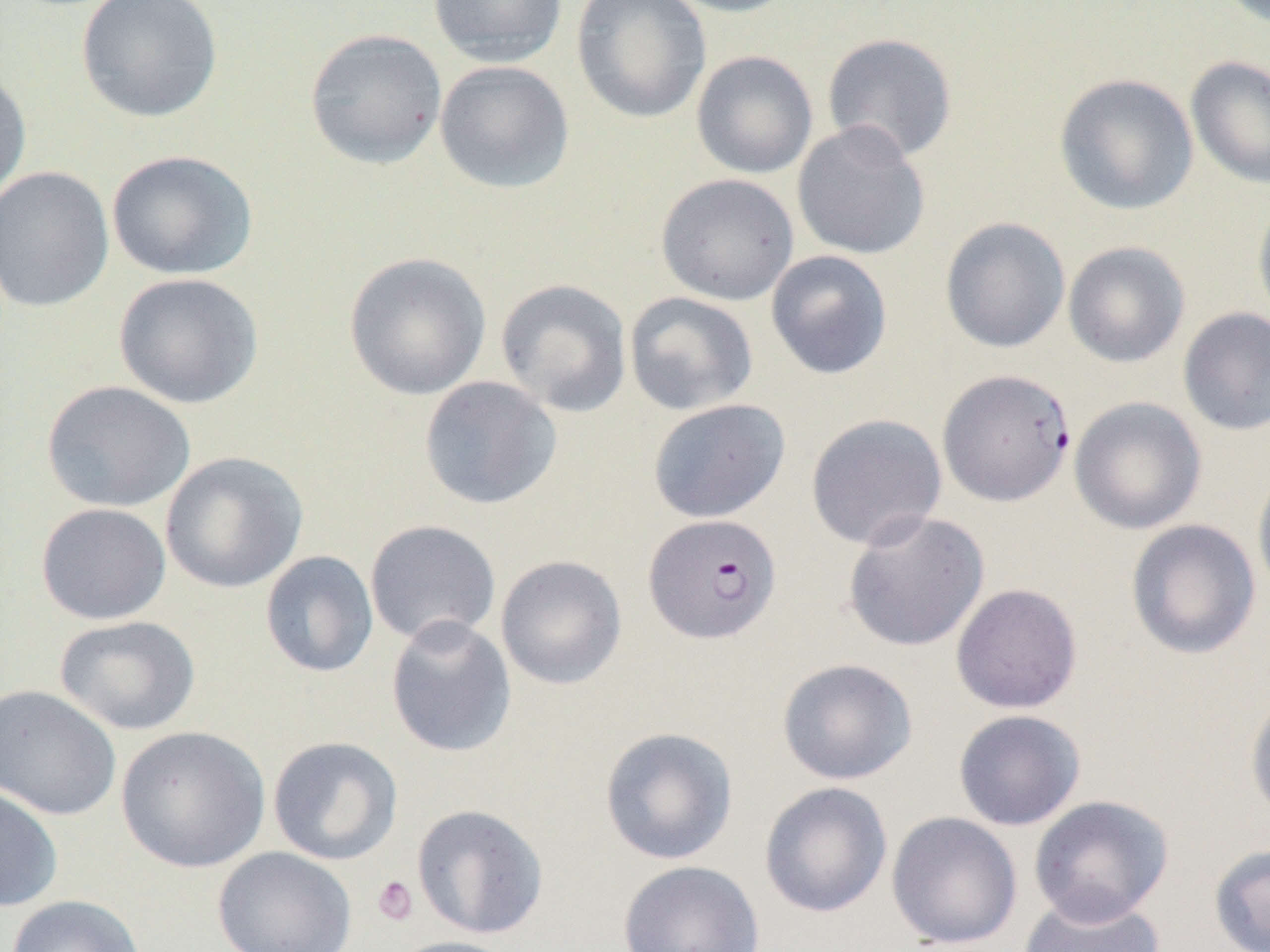
{
  "slide_level_diagnosis": "Plasmodium falciparum",
  "uninfected_red_blood_cell_locations": "approximate bounding boxes as [x1, y1, x2, y2] in pixels: [75, 0, 223, 123], [428, 0, 567, 67], [571, 0, 711, 125], [657, 0, 800, 18], [304, 28, 448, 169], [821, 32, 958, 163], [691, 50, 818, 179], [1185, 55, 1270, 190], [434, 60, 575, 195], [0, 64, 32, 205], [1054, 73, 1199, 216], [792, 121, 931, 260], [106, 149, 258, 281], [0, 166, 115, 313], [655, 173, 799, 306], [1252, 193, 1270, 330], [939, 217, 1071, 353], [1063, 241, 1190, 368], [765, 250, 893, 380], [344, 252, 491, 401], [113, 272, 263, 409], [495, 278, 632, 418], [623, 291, 759, 416], [1177, 306, 1270, 436], [418, 376, 562, 510], [41, 380, 196, 512], [1069, 396, 1207, 535], [646, 398, 791, 524], [805, 413, 947, 551], [160, 451, 308, 594], [1252, 460, 1270, 606], [34, 502, 172, 625], [841, 510, 990, 652], [1125, 518, 1262, 660], [364, 519, 501, 647], [259, 550, 379, 678], [495, 555, 628, 690], [950, 582, 1082, 714], [55, 615, 201, 736], [385, 615, 517, 758], [776, 657, 918, 785], [0, 684, 122, 821], [1245, 688, 1270, 825], [953, 709, 1086, 831], [115, 725, 270, 873], [599, 726, 739, 866], [267, 736, 404, 865], [759, 781, 893, 918], [0, 784, 63, 913], [1028, 794, 1174, 926], [411, 803, 549, 939], [886, 811, 1023, 950], [1208, 843, 1270, 952], [212, 846, 357, 952], [617, 859, 765, 952], [1017, 892, 1165, 952], [6, 894, 146, 952], [387, 936, 524, 952]",
  "platelet_locations": "approximate bounding boxes as [x1, y1, x2, y2] in pixels: [372, 875, 418, 926]",
  "plasmodium_falciparum_infected_red_blood_cell_locations": "approximate bounding boxes as [x1, y1, x2, y2] in pixels: [937, 368, 1076, 508], [643, 513, 781, 645]",
  "modality": "light microscopy",
  "magnification": "1000x",
  "field_of_view": "single",
  "preparation": "thin blood film",
  "image_size": "1270×952 pixels"
}